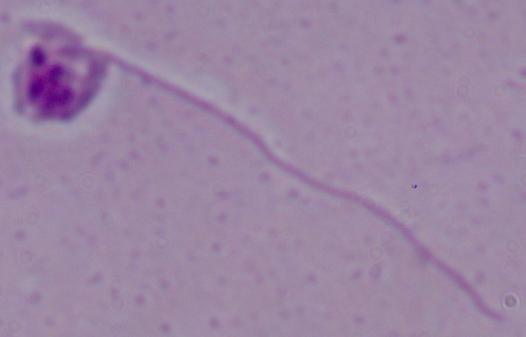

identification = Leishmania
modality = micrograph
magnification = 1000x